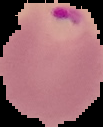
Summary:
  - Malaria status: parasitized
  - Image type: cell region segmented out of the field of view; surrounding area masked to black
  - Image size: 103×127 pixels
  - Preparation: thin blood film